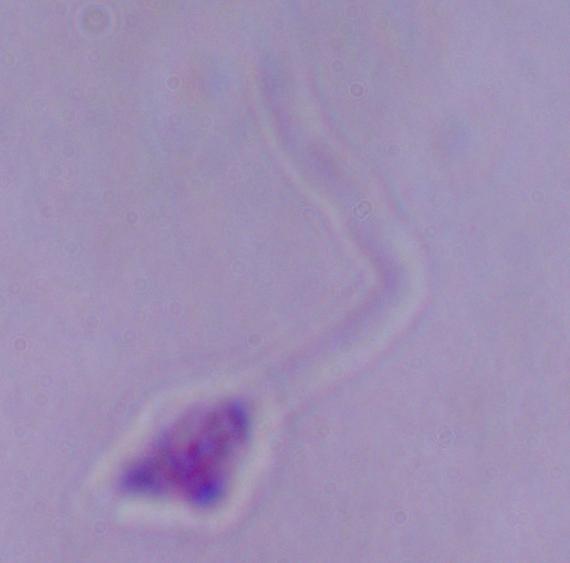

magnification = 1000x
identification = Leishmania
modality = photomicrograph